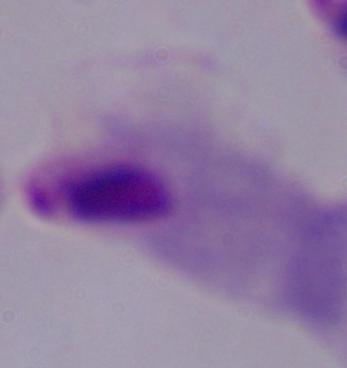
A trichomonad is shown. Photomicrograph. Captured at 1000x magnification.